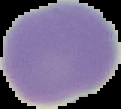
Result: no Plasmodium parasites seen. Image is 121×109 pixels. Segmented cell region on a black background. From a thin blood smear.